State the preparation type.
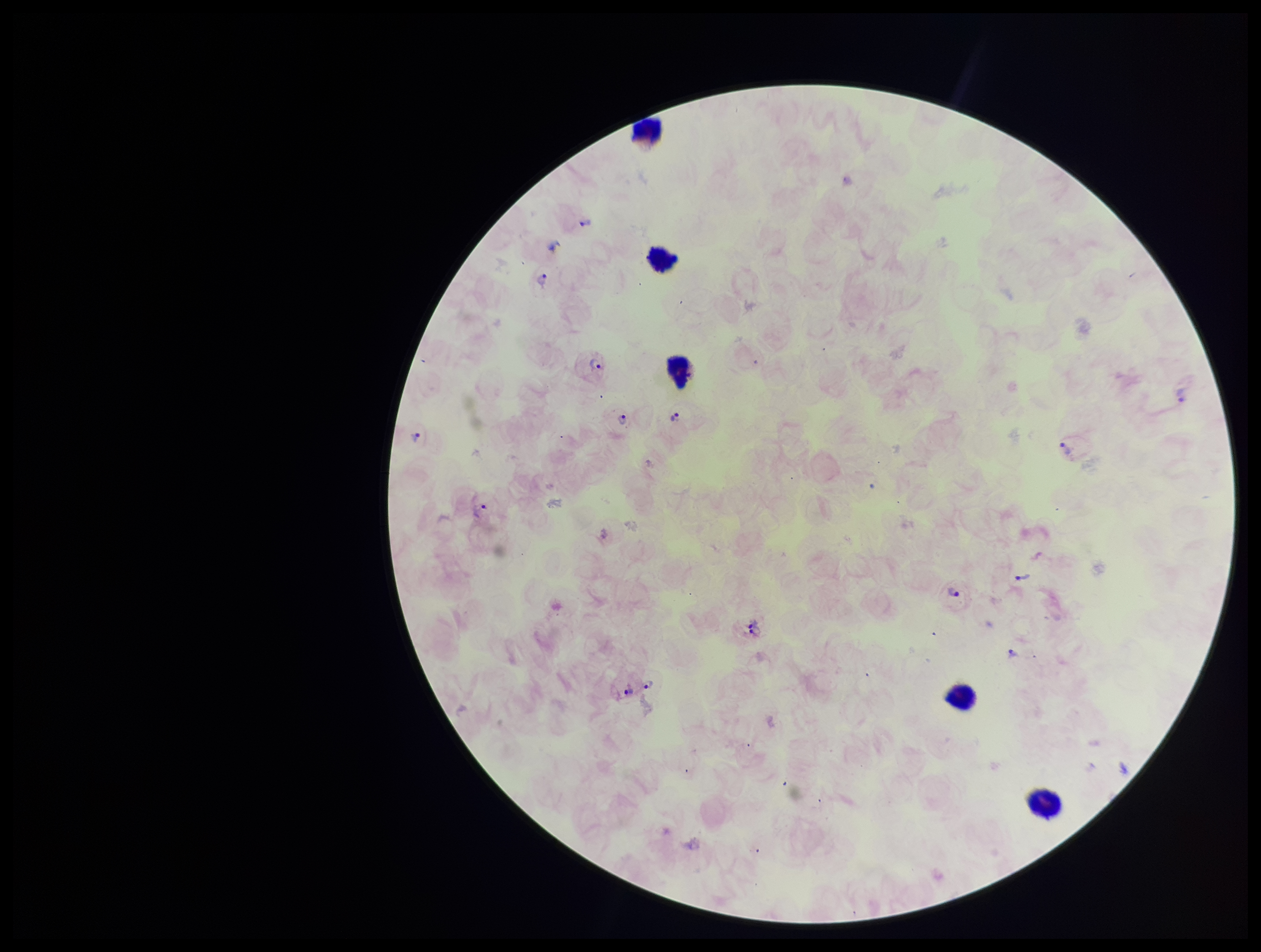

A thick smear.

field of view = single
species reported for this patient = Plasmodium vivax
Plasmodium parasites = detected
capture = smartphone photograph through the microscope eyepiece
leukocyte count = 5
patient malaria status = positive
image size = 1261×952 pixels
stain = Giemsa
parasite count = 11